Report the malaria status.
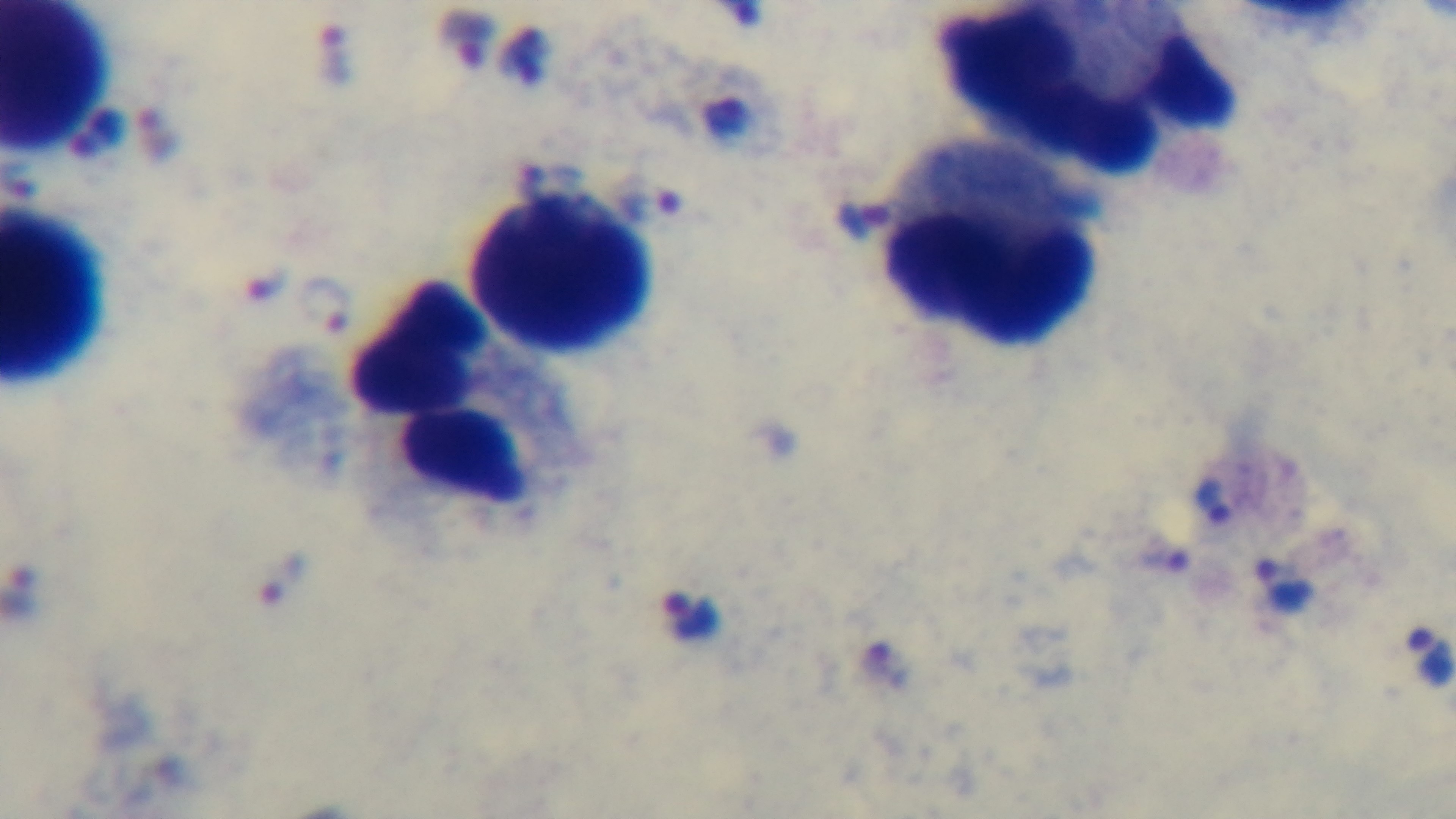

It is infected.

stain: Giemsa
field_of_view: single
preparation: thick blood film
capture: mounted 4K digital camera
modality: light microscopy
objective: 100x oil immersion